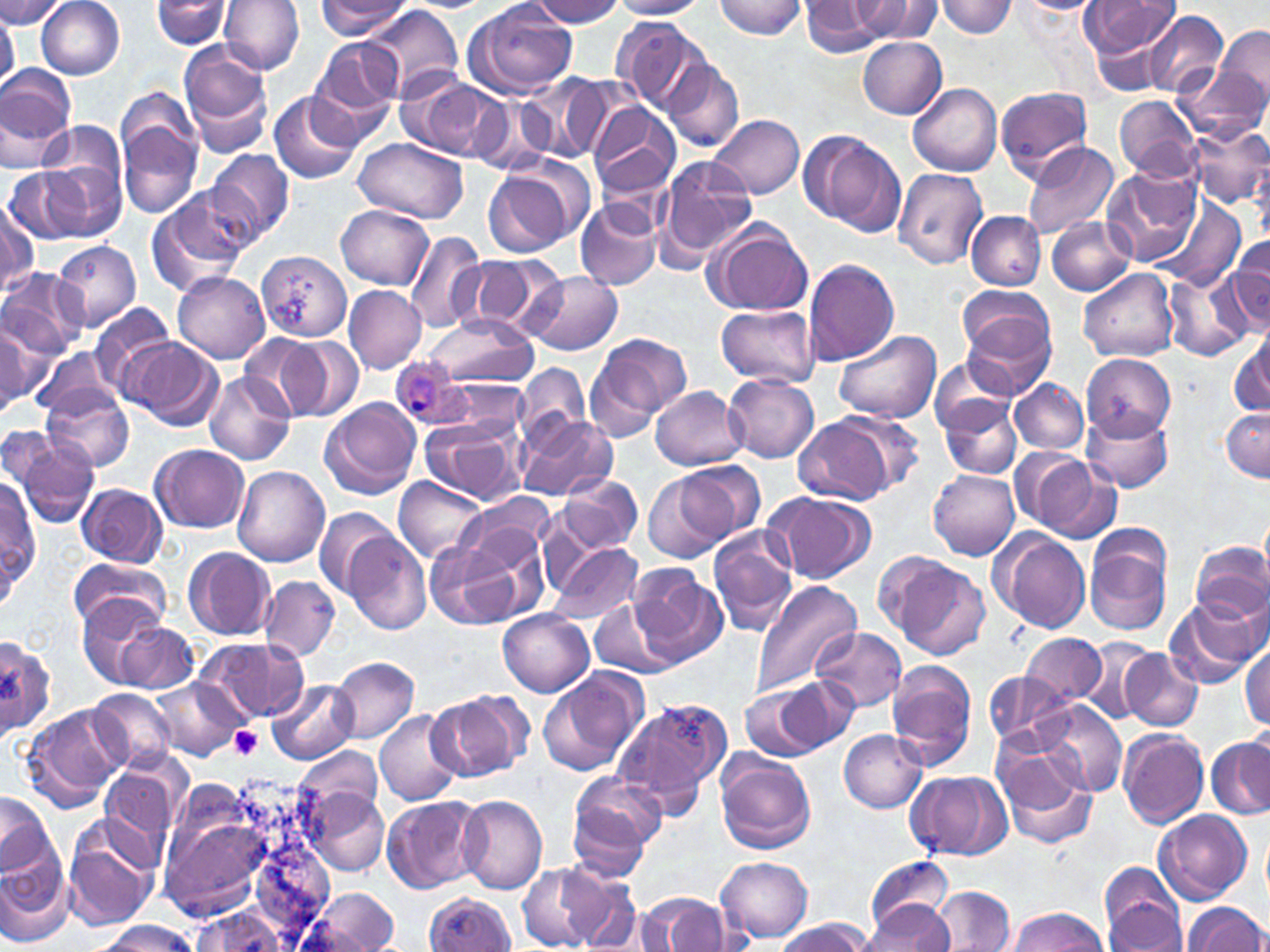
slide-level diagnosis = Plasmodium ovale
platelet locations = approximate bounding boxes as [x1, y1, x2, y2] in pixels: [229, 725, 263, 758]
uninfected red blood cell locations = approximate bounding boxes as [x1, y1, x2, y2] in pixels: [37, 0, 125, 79], [152, 0, 234, 49], [218, 0, 303, 74], [530, 0, 626, 27], [608, 0, 707, 19], [713, 0, 807, 38], [799, 0, 890, 55], [849, 0, 942, 42], [935, 0, 1018, 37], [0, 1, 70, 29], [316, 1, 412, 40], [464, 1, 577, 98], [1012, 1, 1103, 15], [1080, 2, 1181, 60], [364, 4, 465, 98], [1142, 10, 1229, 100], [0, 17, 17, 94], [613, 17, 713, 118], [1214, 23, 1270, 118], [312, 36, 406, 123], [856, 36, 946, 117], [179, 43, 275, 157], [663, 59, 744, 153], [1178, 60, 1267, 147], [0, 61, 77, 158], [519, 76, 608, 159], [404, 77, 506, 162], [908, 82, 1003, 177], [995, 85, 1094, 180], [269, 91, 363, 185], [115, 92, 203, 222], [468, 93, 555, 175], [1114, 96, 1200, 181], [587, 102, 680, 199], [709, 114, 805, 199], [1186, 122, 1270, 214], [41, 124, 129, 206], [800, 130, 906, 237], [352, 136, 469, 224], [1022, 141, 1121, 241], [206, 149, 294, 245], [653, 154, 757, 269], [47, 159, 125, 242], [482, 160, 587, 257], [5, 166, 90, 245], [1103, 167, 1201, 266], [893, 168, 989, 269], [147, 191, 251, 294], [575, 198, 662, 291], [1, 200, 38, 295], [1156, 201, 1246, 291], [336, 205, 432, 289], [966, 211, 1047, 290], [1047, 215, 1136, 295], [703, 218, 815, 316], [405, 230, 486, 334], [1227, 234, 1270, 327], [53, 241, 142, 330], [258, 250, 352, 340], [457, 253, 565, 337], [803, 257, 900, 366], [1078, 268, 1179, 362], [0, 269, 89, 358], [171, 270, 270, 363], [522, 271, 624, 356], [1164, 272, 1253, 362], [957, 284, 1053, 364], [343, 285, 427, 372], [89, 302, 176, 396], [715, 304, 821, 388], [963, 312, 1058, 397], [424, 314, 540, 388], [0, 322, 39, 411], [1231, 329, 1270, 418], [831, 330, 941, 424], [238, 333, 325, 419], [594, 333, 692, 422], [119, 337, 224, 431], [279, 337, 364, 422], [33, 344, 117, 419], [1082, 353, 1175, 439], [585, 356, 667, 444], [930, 359, 1019, 435], [516, 363, 590, 443], [206, 371, 295, 465], [724, 375, 820, 463], [440, 379, 534, 440], [1011, 379, 1088, 454], [651, 386, 747, 470], [42, 387, 133, 472], [319, 397, 422, 499], [939, 397, 1022, 478], [1221, 406, 1270, 481], [1079, 407, 1174, 493], [836, 412, 927, 496], [518, 413, 614, 502], [793, 416, 897, 504], [419, 418, 522, 505], [0, 424, 57, 491], [14, 436, 98, 527], [151, 445, 249, 531], [1013, 449, 1117, 542], [678, 460, 765, 542], [233, 466, 330, 566], [929, 469, 1020, 560], [643, 472, 728, 564], [558, 474, 643, 554], [395, 476, 487, 561], [1, 478, 39, 597], [78, 482, 166, 567], [216, 490, 319, 630], [762, 491, 876, 583], [314, 506, 397, 593], [455, 507, 552, 614], [991, 529, 1091, 633], [707, 530, 798, 636], [1084, 531, 1172, 636], [344, 532, 432, 633], [425, 540, 522, 630], [1190, 541, 1270, 626], [548, 542, 642, 624], [183, 546, 276, 641], [888, 555, 991, 660], [69, 556, 169, 634], [629, 566, 727, 666], [260, 577, 339, 659], [754, 579, 863, 700], [75, 594, 167, 686], [591, 597, 681, 680], [1164, 599, 1259, 690], [498, 610, 595, 697], [117, 621, 198, 694], [812, 628, 907, 713], [1020, 633, 1108, 704], [0, 634, 53, 737], [190, 636, 308, 727], [1081, 637, 1161, 724], [1241, 641, 1270, 730], [1120, 648, 1203, 731], [331, 657, 419, 745], [886, 660, 978, 771], [538, 667, 648, 778], [984, 669, 1069, 747], [775, 675, 856, 752], [268, 679, 356, 765], [156, 680, 244, 762], [740, 684, 826, 758], [89, 689, 178, 773], [427, 689, 531, 781], [613, 698, 731, 813], [1037, 700, 1126, 798], [23, 704, 127, 810], [374, 709, 462, 806], [1118, 728, 1210, 828], [839, 729, 927, 813], [1208, 736, 1270, 821], [296, 744, 381, 823], [996, 746, 1098, 850], [715, 755, 817, 853], [98, 769, 179, 859], [570, 770, 666, 862], [907, 770, 1012, 862], [155, 775, 327, 930], [306, 787, 390, 878], [1, 791, 56, 878], [382, 794, 487, 893], [457, 795, 547, 894], [568, 804, 652, 882], [1154, 809, 1252, 904], [60, 815, 161, 929], [1261, 826, 1269, 906], [0, 853, 74, 945], [867, 854, 953, 936], [716, 856, 813, 943], [519, 862, 606, 950], [552, 863, 646, 952], [1099, 865, 1188, 951], [313, 887, 401, 952], [932, 888, 1014, 952], [424, 892, 515, 951], [649, 894, 730, 951], [864, 901, 955, 949], [1184, 901, 1268, 952], [1007, 906, 1106, 952], [184, 908, 297, 951], [96, 920, 195, 952], [775, 920, 875, 952]
stain = May-Grünwald-Giemsa
magnification = 1000x
preparation = thin blood film
image size = 1270×952 pixels
Plasmodium ovale-infected red blood cell locations = approximate bounding boxes as [x1, y1, x2, y2] in pixels: [388, 357, 471, 429]
modality = optical microscopy
field of view = single